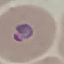
Summary:
  - Malaria status: parasitized
  - Preparation: thin blood smear
  - Stain: Giemsa
  - Image type: automatically extracted cell patch, resized to 64 × 64 pixels
  - Capture: smartphone through the microscope eyepiece